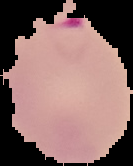

image type = cell region segmented out of the field of view; surrounding area masked to black
image size = 133×166 pixels
preparation = thin blood smear
malaria status = parasitized